Classify this cell by malaria status.
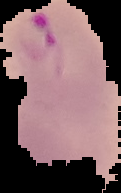

It is parasitized.

Summary:
  - Preparation: thin blood smear
  - Image type: cell region segmented out of the field of view; surrounding area masked to black
  - Image size: 121×193 pixels